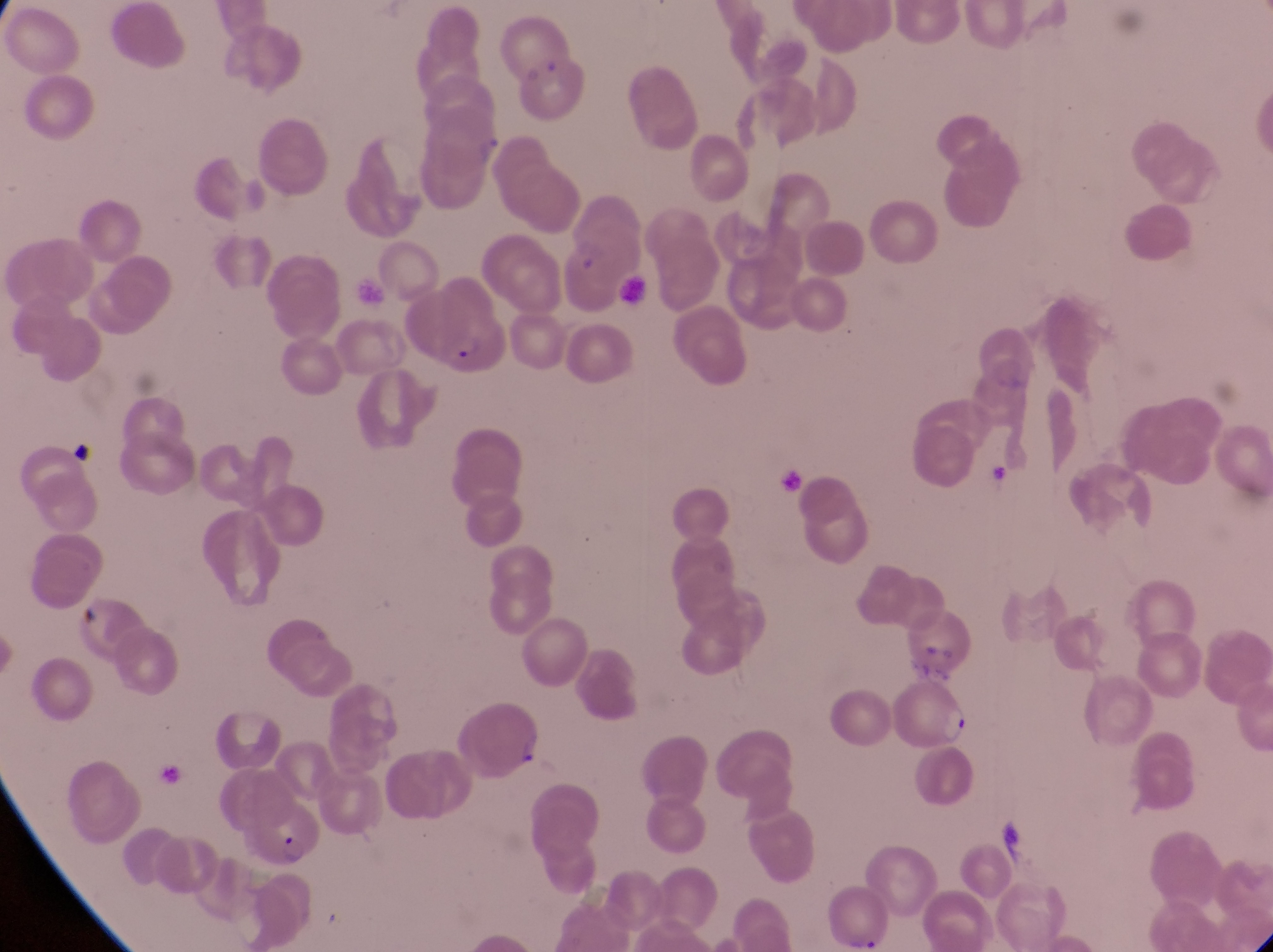

field of view = single
preparation = thin blood smear
parasitised red blood cell locations = approximate bounding boxes as {left, top, right, bottom} in pixels: {400, 300, 508, 378}, {891, 681, 976, 753}, {234, 804, 326, 874}, {831, 883, 894, 951}
artifact (platelet-like body, stain precipitate, or debris) locations = approximate bounding boxes as {left, top, right, bottom} in pixels: {535, 53, 570, 88}, {75, 607, 107, 639}
capture = smartphone photograph through the eyepiece of an Olympus CX-23 microscope
country = Uganda
image size = 1273×952 pixels
magnification = 1000x